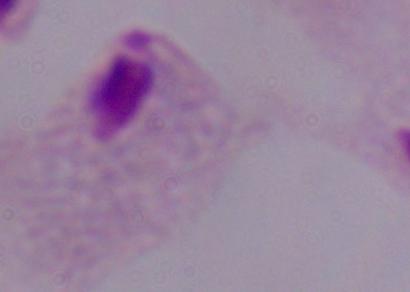

A trichomonad is shown. Photomicrograph. Captured at 1000x magnification.